Locate every blood parasite and identify its species.
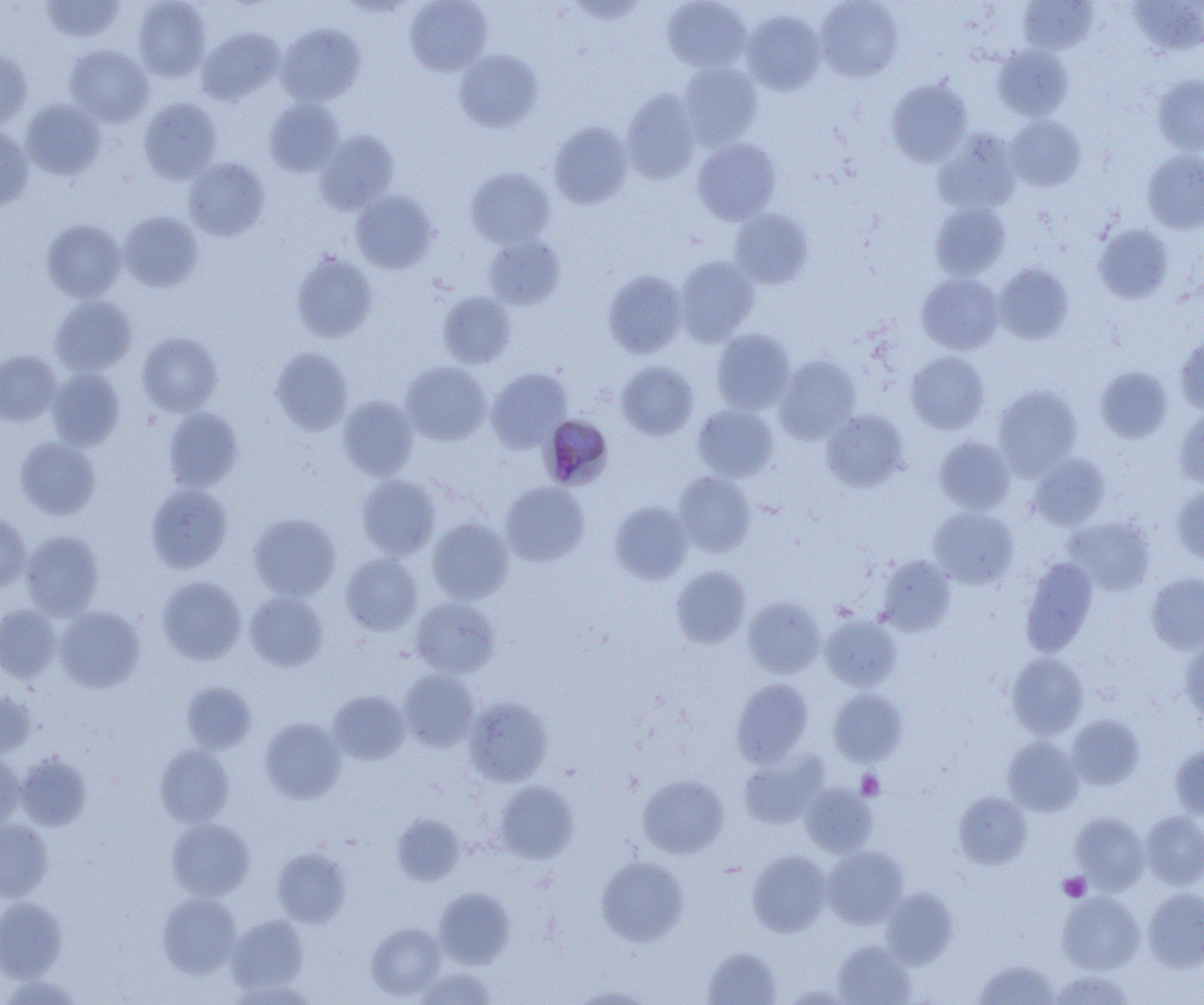
Approximate bounding boxes as (x1, y1, x2, y2) in pixels.
Plasmodium malariae-infected red blood cells: (540, 414, 614, 490).
No Plasmodium falciparum, Plasmodium ovale, Plasmodium vivax, Babesia divergens, or Trypanosoma brucei observed.

Summary:
  - Platelet locations: (856, 771, 884, 800), (1058, 872, 1091, 902)
  - Uninfected red blood cell locations: (40, 0, 125, 42), (405, 0, 493, 76), (662, 0, 751, 73), (815, 0, 904, 82), (131, 1, 210, 81), (1018, 1, 1098, 54), (1124, 1, 1204, 58), (743, 11, 826, 95), (277, 23, 365, 106), (197, 28, 284, 105), (64, 45, 154, 126), (992, 45, 1074, 120), (0, 49, 33, 129), (454, 49, 544, 132), (678, 61, 763, 147), (1152, 74, 1204, 156), (887, 78, 973, 167), (621, 89, 702, 184), (139, 98, 222, 183), (264, 98, 343, 176), (21, 99, 106, 180), (1006, 115, 1085, 191), (548, 121, 633, 208), (0, 124, 34, 210), (314, 131, 399, 214), (933, 131, 1022, 214), (692, 137, 781, 225), (1142, 149, 1204, 234), (183, 157, 270, 241), (465, 167, 554, 247), (351, 190, 438, 273), (930, 202, 1010, 280), (729, 209, 813, 288), (119, 211, 202, 291), (42, 219, 126, 302), (1093, 223, 1174, 303), (482, 234, 565, 310), (291, 252, 378, 343), (675, 256, 759, 345), (993, 263, 1074, 345), (603, 270, 688, 358), (916, 272, 1004, 355), (438, 291, 516, 368), (50, 295, 137, 375), (711, 329, 795, 414), (137, 331, 223, 416), (1175, 333, 1204, 415), (270, 347, 353, 435), (0, 350, 61, 425), (905, 351, 990, 434), (775, 355, 861, 444), (400, 361, 491, 445), (617, 361, 699, 440), (1094, 365, 1174, 444), (47, 367, 125, 450), (486, 367, 572, 452), (993, 385, 1082, 478), (338, 396, 419, 479), (693, 403, 779, 481), (163, 406, 244, 491), (1174, 407, 1204, 488), (821, 409, 909, 491), (934, 436, 1016, 514), (14, 437, 101, 519), (1028, 452, 1110, 530), (673, 471, 756, 557), (356, 475, 441, 560), (500, 481, 589, 566), (145, 483, 233, 572), (1171, 484, 1204, 565), (609, 501, 694, 584), (928, 507, 1018, 589), (0, 513, 31, 591), (248, 513, 340, 600), (1063, 516, 1156, 595), (427, 518, 514, 604), (21, 530, 105, 618), (340, 553, 423, 635), (876, 556, 956, 636), (1019, 557, 1098, 656), (671, 565, 751, 648), (1146, 572, 1204, 654), (157, 576, 246, 664), (244, 591, 329, 671), (743, 596, 824, 678), (409, 597, 501, 678), (0, 604, 61, 683), (55, 606, 145, 692), (820, 615, 901, 691), (1180, 638, 1204, 724), (1007, 652, 1088, 738), (398, 670, 479, 751), (731, 678, 813, 766), (181, 681, 257, 753), (828, 688, 907, 766), (0, 690, 38, 757), (328, 690, 411, 764), (464, 697, 553, 786), (1067, 714, 1145, 789), (259, 717, 347, 804), (1002, 736, 1083, 816), (155, 745, 234, 827), (1169, 745, 1204, 820), (0, 749, 23, 833), (738, 750, 829, 829), (17, 752, 92, 830), (637, 774, 729, 859), (494, 781, 579, 864), (801, 782, 876, 857), (954, 792, 1032, 869), (1071, 812, 1149, 893), (1140, 812, 1204, 889), (392, 814, 464, 885), (166, 818, 255, 901), (0, 820, 53, 902), (822, 846, 908, 928), (272, 848, 351, 927), (747, 850, 832, 936), (597, 856, 689, 947), (1142, 887, 1204, 972), (434, 888, 515, 969), (882, 888, 958, 967), (1057, 891, 1144, 974), (157, 892, 242, 978), (0, 898, 67, 980), (227, 915, 309, 994), (365, 923, 446, 1000), (832, 940, 916, 1005), (703, 947, 781, 1005), (974, 958, 1060, 1004), (415, 967, 498, 1004), (1050, 971, 1135, 1005), (782, 983, 858, 1004), (569, 985, 657, 1004)
  - Slide-level diagnosis: Plasmodium malariae
  - Modality: optical microscopy
  - Image size: 1204×1005 pixels
  - Field of view: one of a larger specimen
  - Preparation: thin blood smear
  - Magnification: 1000x